Point out each leukocyte.
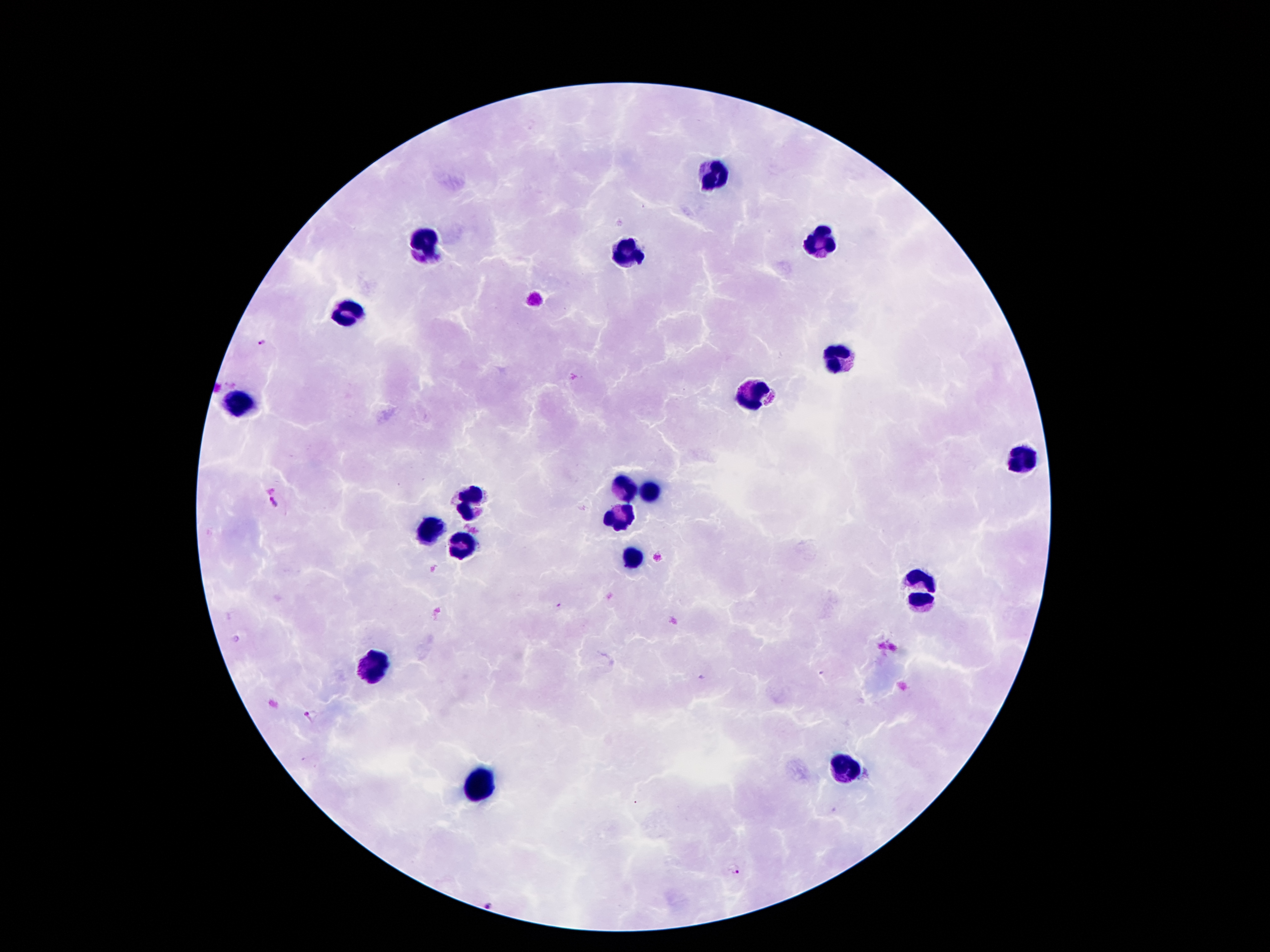

Approximate centers as (x, y) in pixels.
Leukocytes: (717, 174), (817, 241), (424, 243), (629, 255), (348, 309), (839, 358), (750, 394), (238, 404), (1020, 455), (624, 485), (654, 493), (473, 502), (621, 518), (427, 528), (463, 543), (631, 556), (917, 589), (372, 670), (847, 770), (473, 785).

Summary:
  - Malaria parasite locations: (265, 341), (274, 503), (310, 714), (735, 871), (490, 907)
  - Preparation: thick blood smear
  - Patient malaria status: infected with Plasmodium falciparum
  - Field of view: single
  - Magnification: 100x
  - Stain: Giemsa
  - Capture: smartphone through the microscope eyepiece
  - Image size: 1270×952 pixels